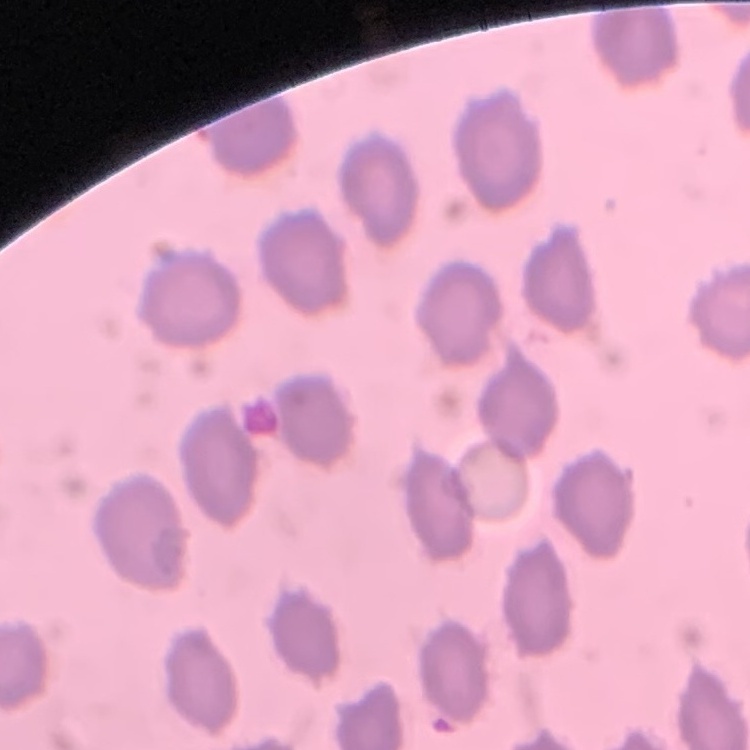

red blood cell morphology = no rouleaux formation
preparation = thin peripheral smear
image type = square crop of a larger photomicrograph
stain = Field's or Giemsa